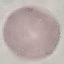
result = no malaria parasites detected
stain = Giemsa
preparation = thin blood film
capture = smartphone through the microscope eyepiece
image type = cell patch, automatically extracted from a larger field of view and resized to 64 × 64 pixels